Name the parasite shown.
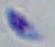

This is Toxoplasma gondii.

Micrograph. Captured at 1000x magnification.